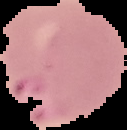

result = malaria parasites identified
image type = cell region segmented out of the field of view; surrounding area masked to black
image size = 127×130 pixels
preparation = thin blood smear